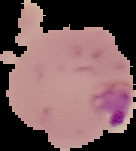

Malaria status: parasitized. From a thin blood film. Image is 136×151 pixels. Segmented cell region on a black background.